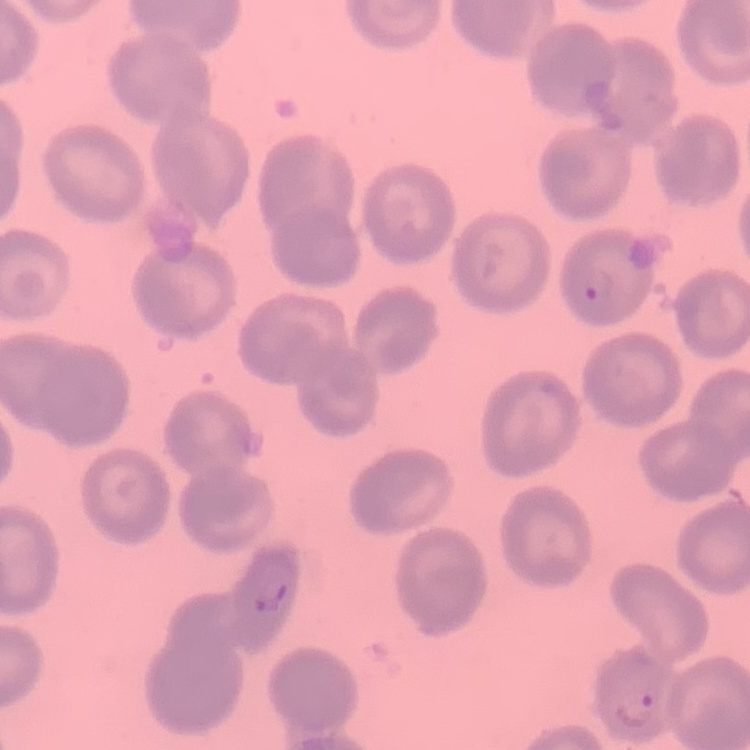

Summary:
  - Red blood cell morphology: no rouleaux formation
  - Preparation: thin blood film
  - Stain: Field's or Giemsa
  - Image type: square crop of a larger photomicrograph